State which cell type is depicted.
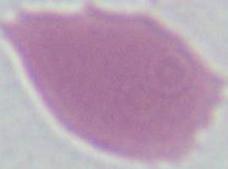
This is an erythrocyte.

Summary:
  - Modality: micrograph
  - Magnification: 1000x